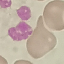

result = no malaria parasites detected
image type = automatically extracted cell patch, resized to 64 × 64 pixels
preparation = thin smear
capture = smartphone through the microscope eyepiece
stain = Giemsa